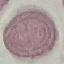
result = negative for malaria parasites
image type = cell patch, automatically extracted from a larger field of view and resized to 64 × 64 pixels
preparation = thin blood film
capture = smartphone camera at the microscope eyepiece
stain = Giemsa